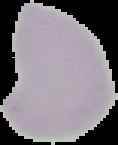

Summary:
  - Image type: segmented cell region on a black background
  - Image size: 118×145 pixels
  - Preparation: thin blood smear
  - Malaria status: uninfected